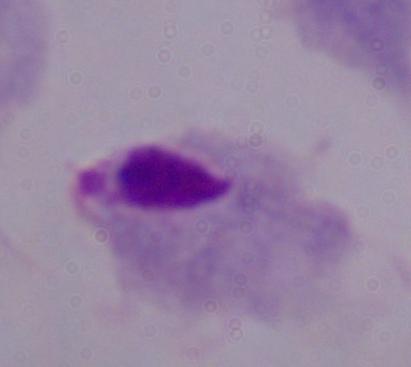
1000x magnification. Photomicrograph. A trichomonad is seen.